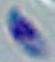 1000x magnification. Toxoplasma gondii is seen. Photomicrograph.